Describe the morphology of the erythrocytes.
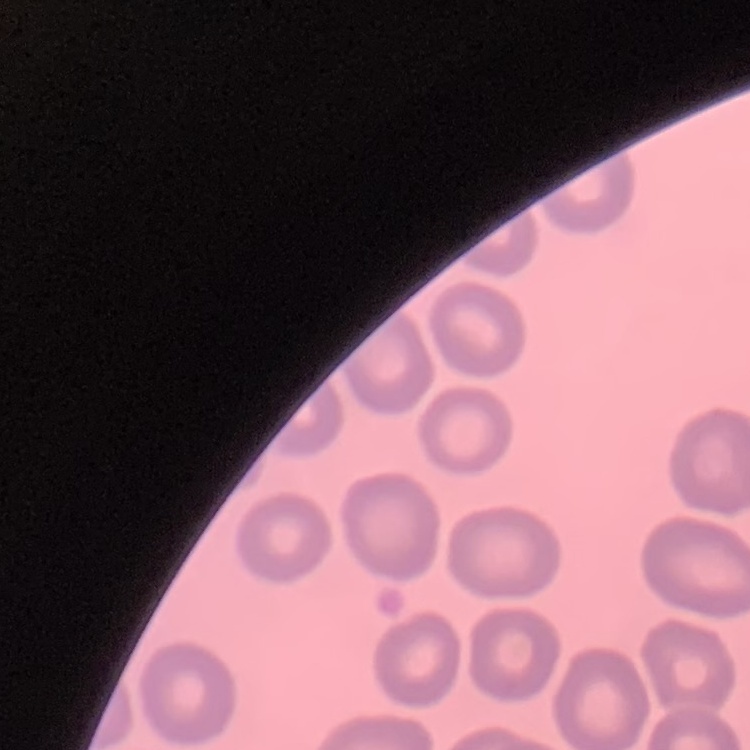

No rouleaux formation.

One tile cut from a larger photomicrograph. Stained with either Field's or Giemsa. Thin blood film.